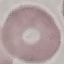
{
  "result": "negative for malaria parasites",
  "capture": "smartphone camera at the microscope eyepiece",
  "stain": "Giemsa",
  "image_type": "automatically extracted cell patch, resized to 64 × 64 pixels",
  "preparation": "thin smear"
}